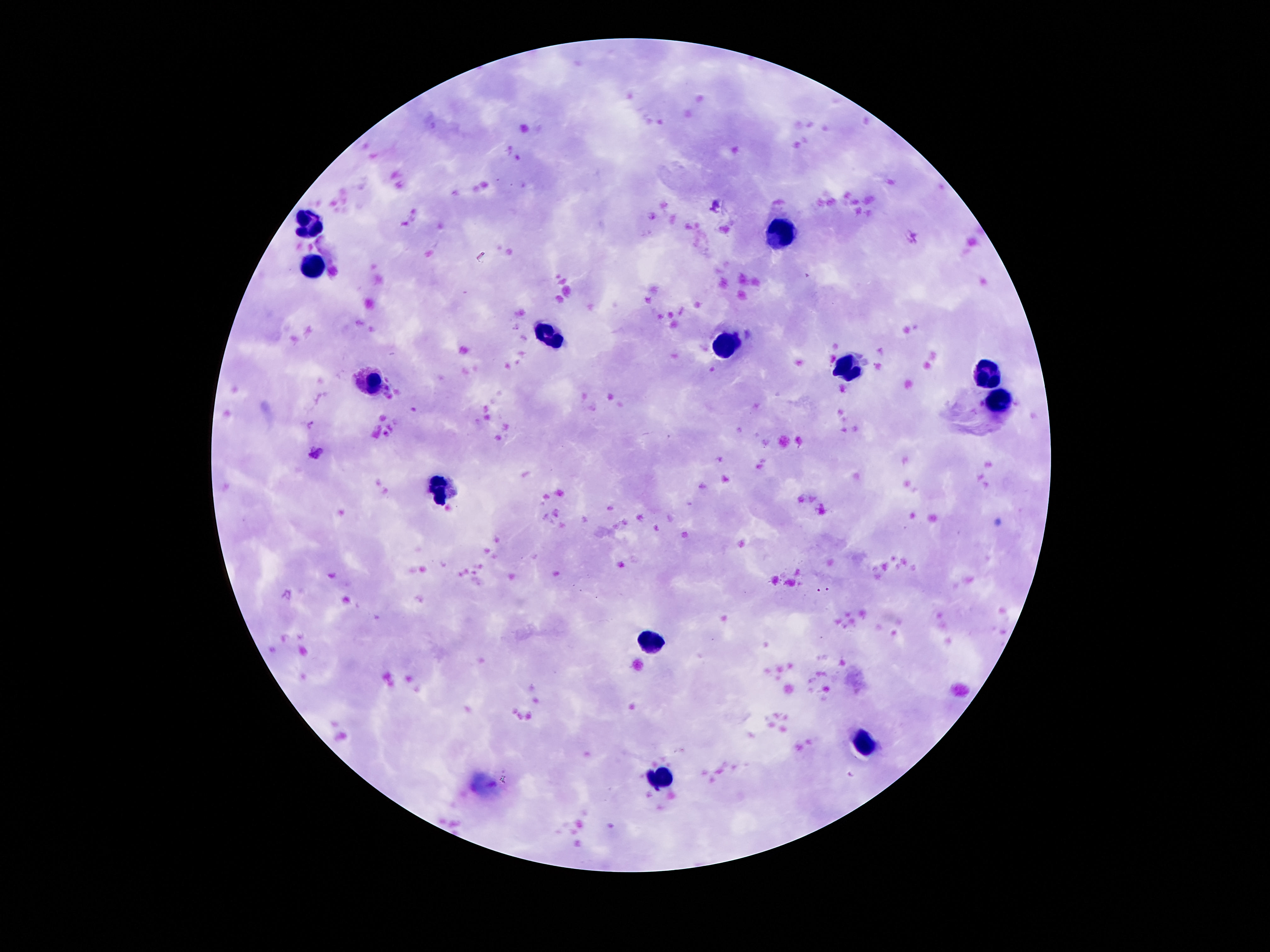

preparation = thick blood smear
field of view = one from this slide
magnification = 100x
patient malaria status = negative
leukocyte locations = approximate object centers, in pixels from the top-left corner: (x=312, y=218), (x=779, y=234), (x=316, y=265), (x=550, y=338), (x=725, y=349), (x=847, y=368), (x=987, y=372), (x=375, y=381), (x=999, y=402), (x=443, y=486), (x=656, y=638), (x=865, y=742), (x=661, y=777)
stain = Giemsa
image size = 1270×952 pixels
capture = smartphone camera through the microscope eyepiece